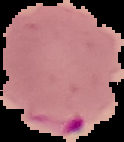
Segmented cell region on a black background. Result: malaria parasites detected. From a thin blood film. Image is 124×142 pixels.